Classify this cell by malaria status.
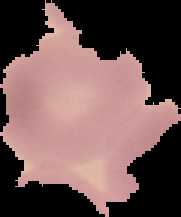
Uninfected.

From a thin blood film. Segmented cell region on a black background. Image is 181×217 pixels.